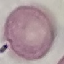 Malaria status: uninfected. Thin blood film. Photographed with a smartphone camera at the microscope eyepiece. Giemsa-stained preparation. Cell patch, automatically extracted from a larger field of view and resized to 64 × 64 pixels.